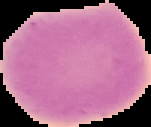 Image is 151×127 pixels. Segmented cell region on a black background. Malaria status: uninfected. From a thin blood smear.